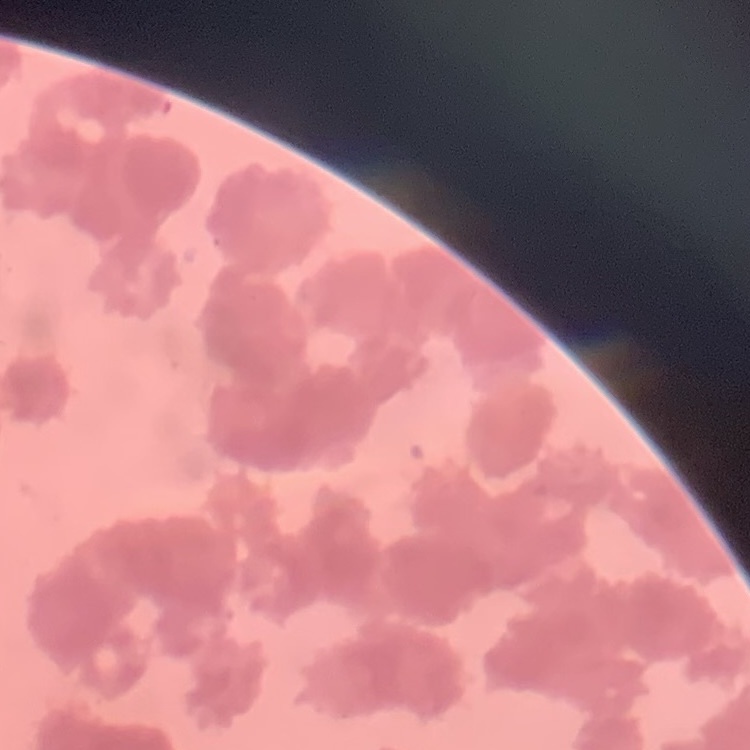

Summary:
  - Erythrocyte morphology: rouleaux formation
  - Image type: square crop of a larger photomicrograph
  - Preparation: thin blood film
  - Stain: Field's or Giemsa